Report the malaria status of this cell.
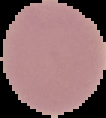
Uninfected.

Summary:
  - Preparation: thin blood film
  - Image size: 106×118 pixels
  - Image type: segmented cell region with the area outside set to black